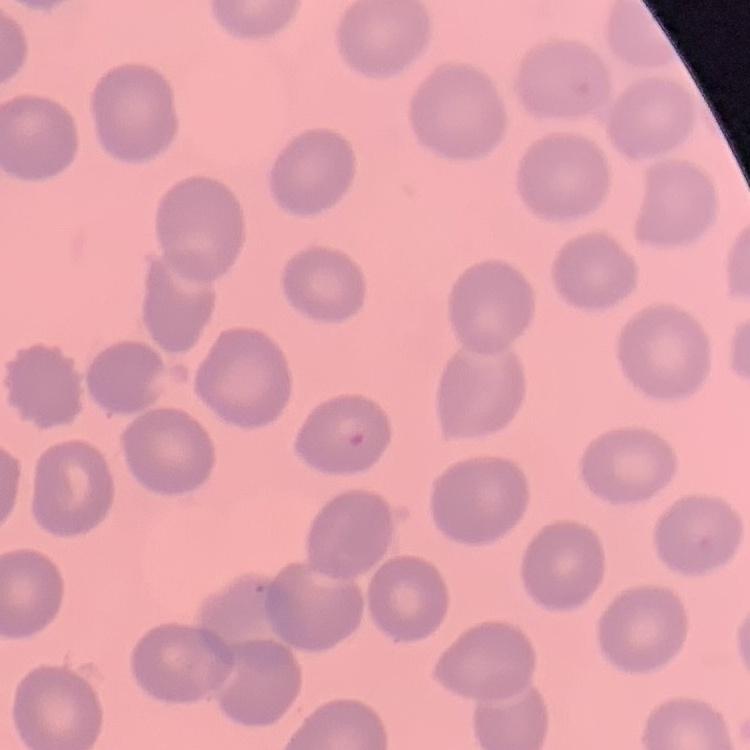
Summary:
  - Red blood cell morphology: no rouleaux formation
  - Preparation: thin blood film
  - Stain: Field's or Giemsa
  - Image type: square crop of a larger photomicrograph